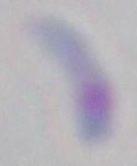

{
  "identification": "Toxoplasma gondii",
  "modality": "micrograph",
  "magnification": "1000x"
}